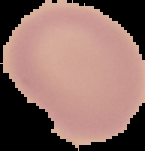
Summary:
  - Preparation: thin blood smear
  - Image size: 145×151 pixels
  - Image type: segmented cell region on a black background
  - Malaria status: uninfected